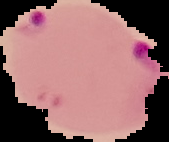
image_size: 169×142 pixels
image_type: segmented cell region with the area outside set to black
malaria_status: parasitized
preparation: thin blood film